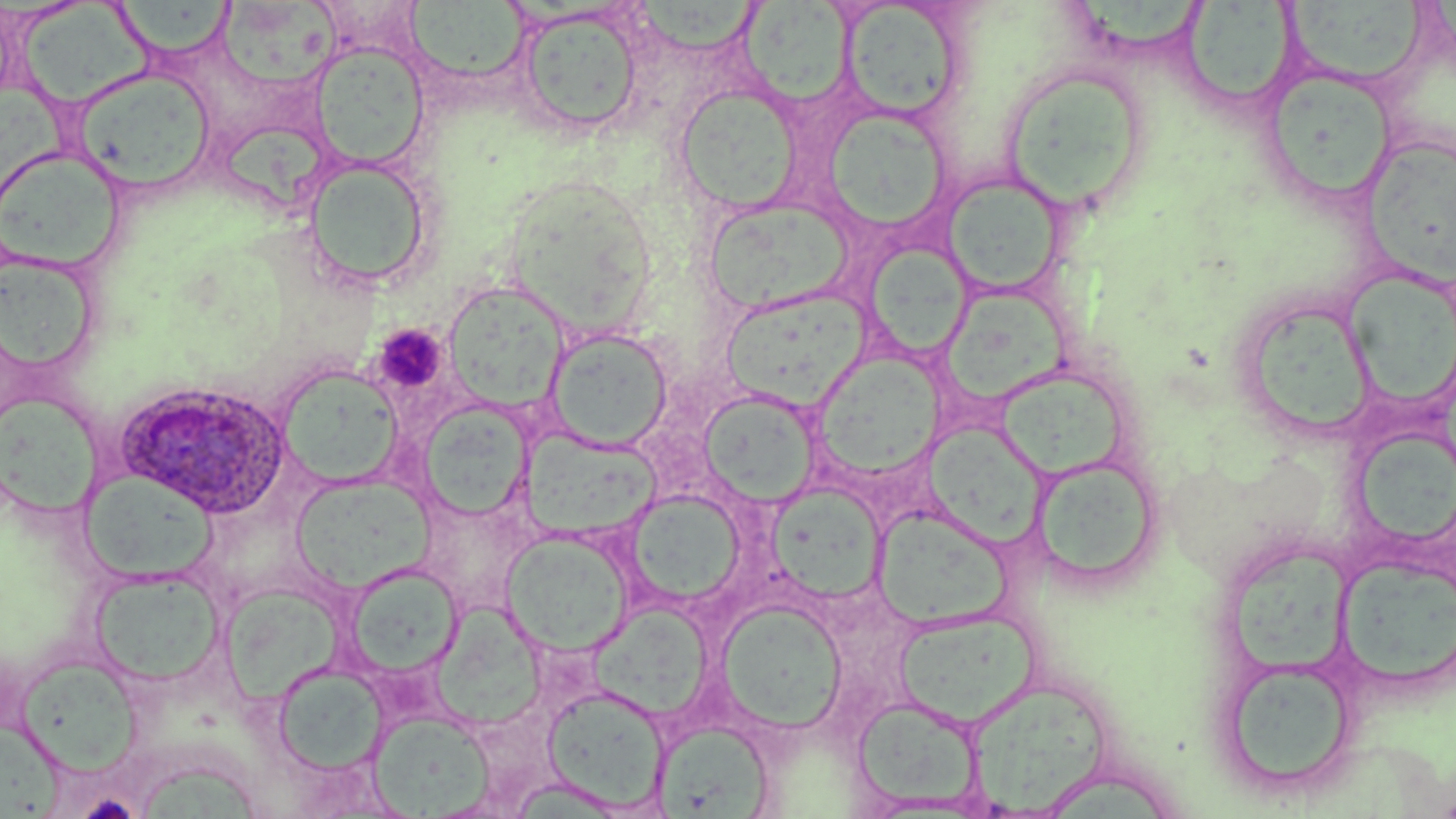
slide-level diagnosis = Plasmodium ovale
stain = May-Grünwald-Giemsa
Plasmodium ovale-infected red blood cell locations = approximate bounding boxes as (x1, y1, x2, y2) in pixels: (117, 382, 290, 518)
modality = optical microscopy
uninfected red blood cell locations = approximate bounding boxes as (x1, y1, x2, y2) in pixels: (113, 0, 236, 62), (634, 0, 763, 57), (1283, 0, 1428, 88), (738, 1, 852, 106), (19, 2, 165, 108), (217, 2, 349, 85), (405, 2, 529, 84), (840, 2, 966, 123), (1075, 2, 1208, 54), (1182, 2, 1297, 112), (516, 7, 645, 135), (311, 42, 429, 168), (1000, 64, 1152, 211), (1261, 67, 1395, 204), (71, 68, 216, 194), (0, 84, 70, 202), (674, 85, 802, 213), (823, 109, 952, 233), (221, 127, 334, 207), (1362, 134, 1456, 285), (0, 146, 125, 272), (303, 158, 434, 289), (942, 174, 1069, 298), (505, 176, 653, 340), (701, 197, 853, 316), (869, 243, 972, 359), (1, 251, 101, 378), (1344, 268, 1456, 414), (440, 279, 571, 415), (945, 282, 1074, 403), (720, 283, 882, 410), (1237, 293, 1378, 442), (545, 327, 674, 451), (814, 352, 942, 481), (276, 364, 404, 489), (995, 373, 1133, 477), (700, 389, 820, 508), (2, 393, 101, 520), (417, 399, 534, 521), (1355, 422, 1456, 550), (924, 423, 1048, 553), (521, 430, 660, 541), (1031, 452, 1163, 591), (71, 470, 221, 585), (291, 475, 433, 593), (767, 482, 888, 604), (625, 490, 748, 608), (871, 505, 1010, 629), (502, 531, 635, 656), (1229, 544, 1354, 675), (1335, 554, 1456, 692), (344, 563, 463, 679), (88, 567, 226, 689), (220, 584, 349, 708), (718, 598, 848, 732), (438, 600, 551, 735), (590, 605, 712, 720), (894, 608, 1041, 728), (14, 654, 146, 776), (1219, 656, 1360, 797), (273, 663, 388, 777), (965, 678, 1113, 813), (543, 684, 670, 812), (852, 695, 985, 811), (369, 709, 494, 817), (654, 721, 777, 817), (0, 722, 75, 819), (138, 763, 263, 819)
platelet locations = approximate bounding boxes as (x1, y1, x2, y2) in pixels: (374, 324, 448, 395)
field of view = one of a larger specimen
preparation = thin blood film
magnification = 1000x
image size = 1456×819 pixels